Identify the preparation type.
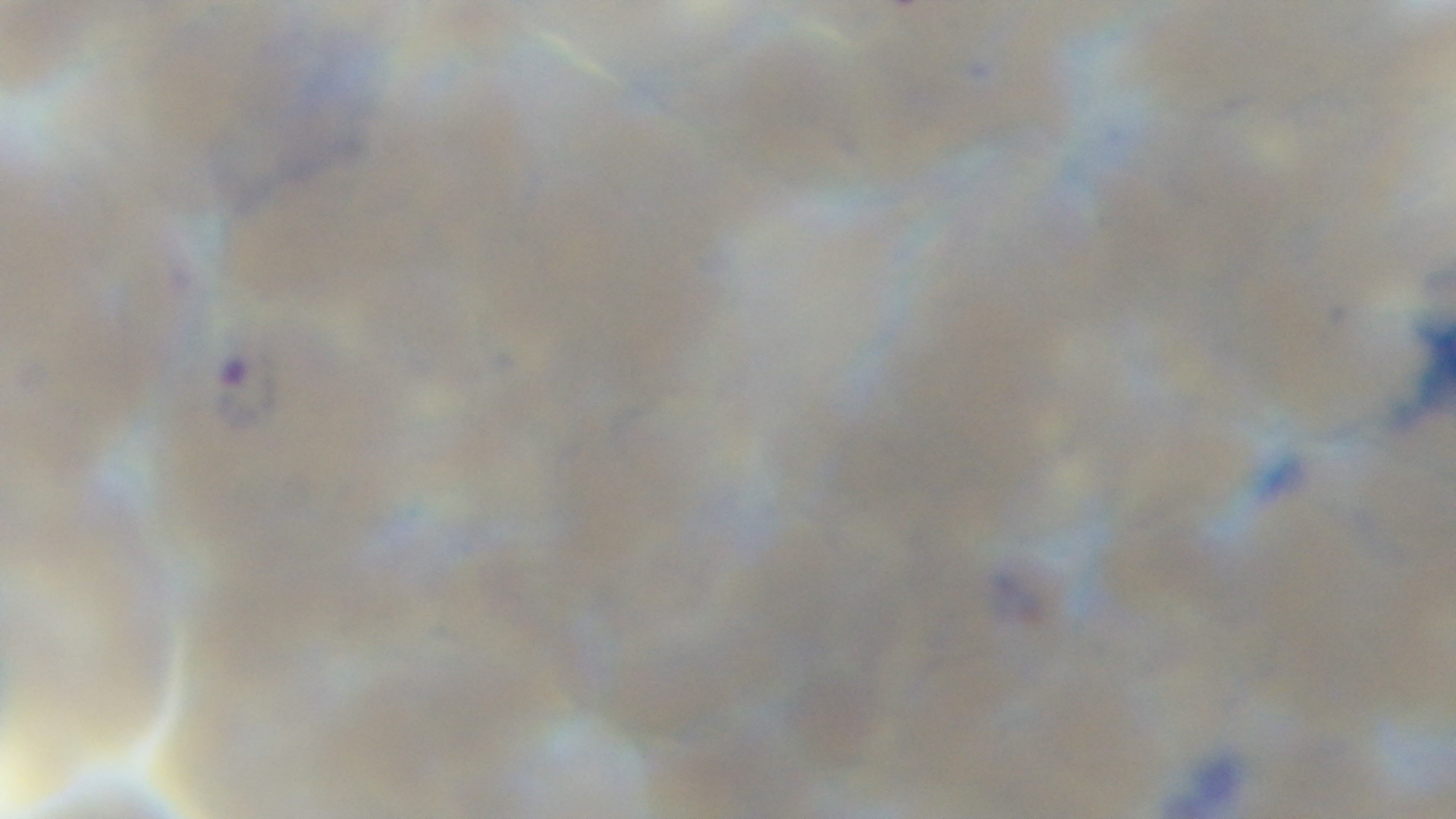

A thin smear.

Single field of view. Captured with a mounted 4K digital camera. Malaria status: infected. Oil-immersion objective, 100x. Giemsa-stained. Photomicrograph.